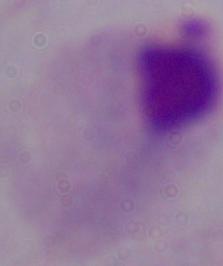
Summary:
  - Identification: trichomonad
  - Magnification: 1000x
  - Modality: micrograph